Describe the morphology of the erythrocytes.
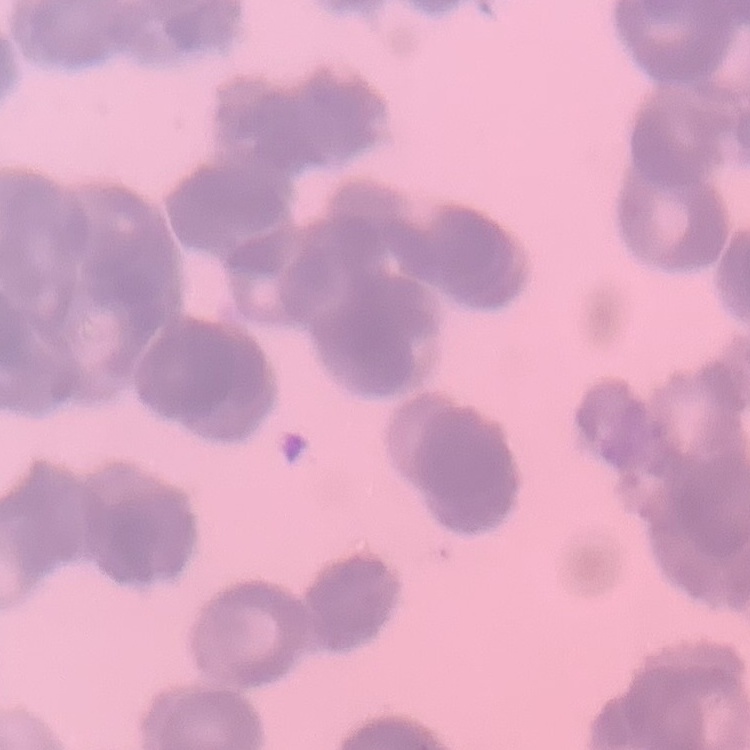

They show rouleaux formation.

{
  "image_type": "square crop of a larger photomicrograph",
  "preparation": "thin blood smear",
  "stain": "Field's or Giemsa"
}